Describe the morphology of the erythrocytes.
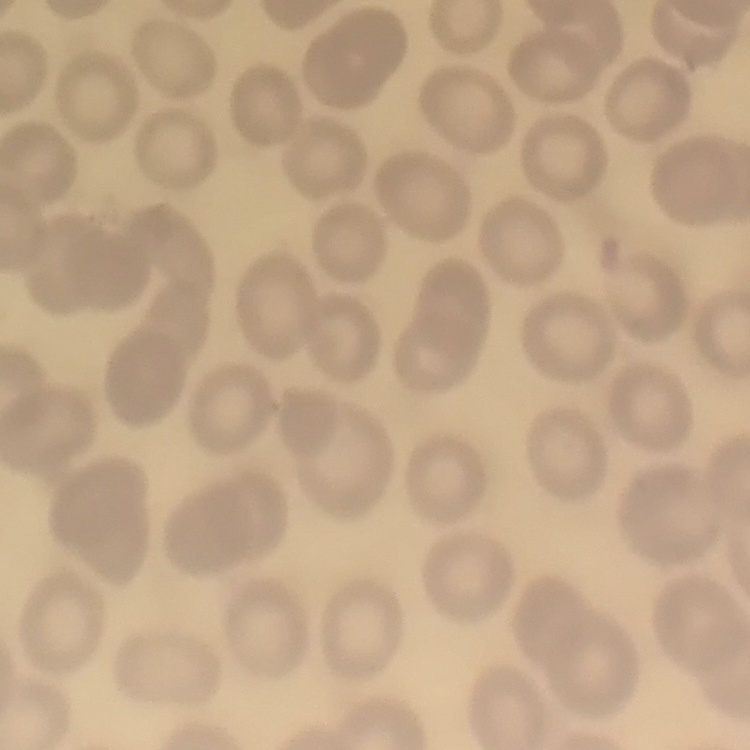
No rouleaux formation.

image type = one tile cut from a larger photomicrograph
preparation = thin peripheral smear
stain = Field's or Giemsa